Identify the parasite.
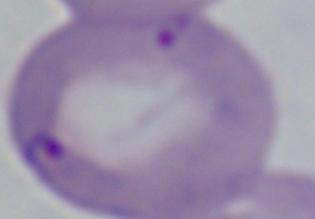
Babesia.

1000x magnification. Photomicrograph.